Classify this cell by malaria status.
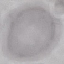
Uninfected.

Summary:
  - Stain: Giemsa
  - Capture: smartphone through the microscope eyepiece
  - Preparation: thin blood film
  - Image type: automatically extracted cell patch, resized to 64 × 64 pixels